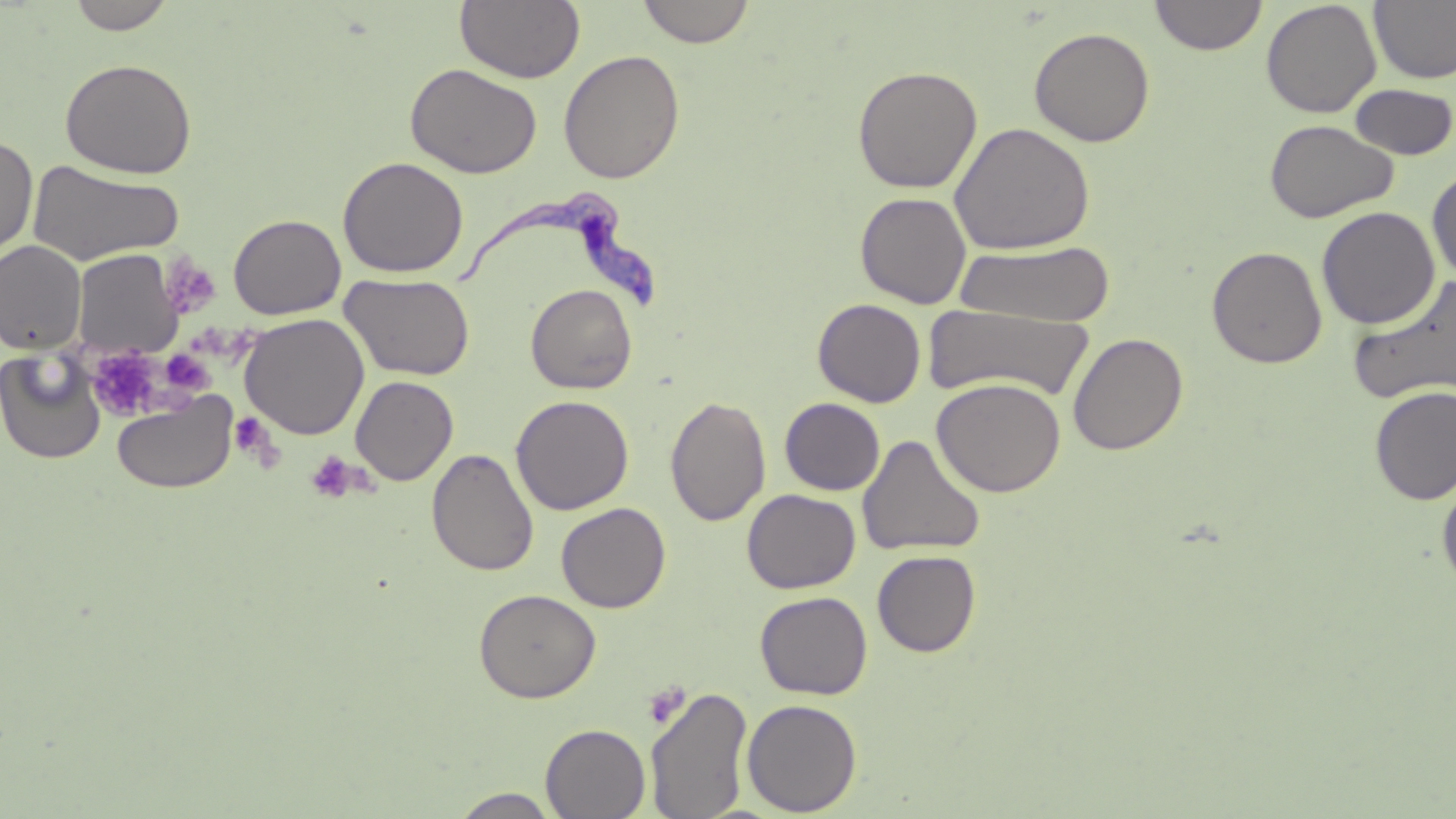

Approximate bounding boxes as (x1, y1, x2, y2) in pixels. Platelet locations: (159, 254, 221, 320), (164, 344, 221, 399), (86, 347, 174, 422), (233, 416, 285, 467), (305, 452, 359, 503). Uninfected red blood cell locations: (67, 0, 177, 34), (455, 0, 585, 83), (637, 0, 756, 48), (1149, 0, 1268, 56), (1369, 0, 1456, 85), (1261, 1, 1382, 118), (1029, 26, 1155, 147), (558, 49, 685, 184), (60, 58, 197, 179), (406, 62, 542, 179), (852, 65, 982, 194), (1348, 83, 1456, 160), (1265, 119, 1398, 223), (949, 122, 1096, 255), (0, 135, 38, 262), (337, 156, 469, 278), (26, 160, 185, 267), (1427, 167, 1456, 282), (855, 191, 972, 309), (1316, 206, 1440, 330), (228, 214, 346, 320), (0, 241, 86, 354), (954, 241, 1117, 326), (1207, 245, 1327, 369), (72, 250, 183, 357), (340, 272, 476, 381), (1348, 274, 1456, 408), (525, 283, 638, 394), (813, 298, 926, 408), (922, 304, 1095, 403), (240, 313, 369, 439), (1067, 331, 1189, 456), (0, 349, 107, 465), (350, 376, 459, 486), (931, 377, 1066, 497), (1369, 386, 1456, 505), (112, 392, 238, 494), (511, 395, 634, 515), (664, 395, 771, 527), (779, 398, 885, 496), (857, 434, 986, 558), (427, 448, 540, 577), (1437, 475, 1456, 594), (742, 489, 860, 594), (555, 503, 671, 613), (872, 550, 981, 657), (474, 588, 601, 703), (755, 591, 873, 700), (646, 684, 753, 819), (741, 698, 862, 816), (541, 723, 650, 818), (450, 788, 562, 818). Trypanosoma brucei locations: (453, 192, 662, 312). Slide-level diagnosis: Trypanosoma brucei. Image is 1456×819 pixels. Thin blood smear. May-Grünwald-Giemsa stain. Optical microscopy. One field of a larger specimen. Captured at 1000x magnification.